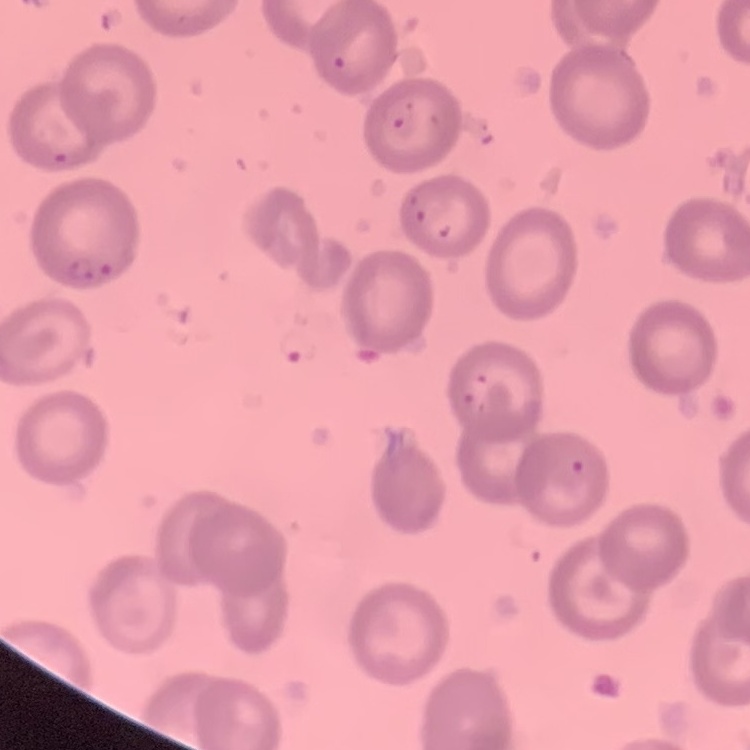
{
  "red_blood_cell_morphology": "no rouleaux formation",
  "stain": "Field's or Giemsa",
  "image_type": "one tile cut from a larger photomicrograph",
  "preparation": "thin blood smear"
}